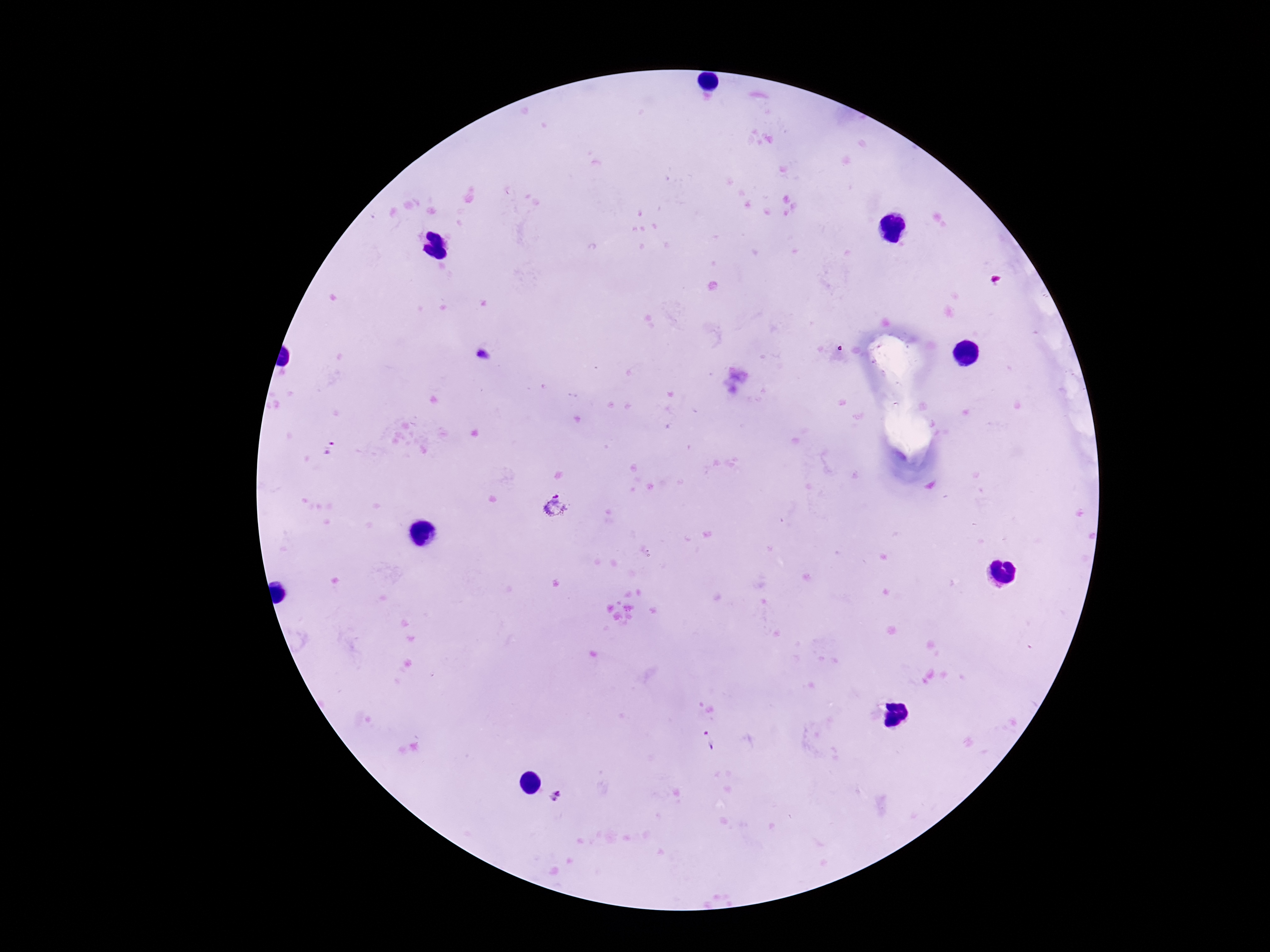

Approximate object centers, in pixels from the top-left corner.
Summary:
  - Plasmodium parasite locations: (x=482, y=356), (x=554, y=506), (x=709, y=740), (x=557, y=795)
  - Field of view: one from this slide
  - Patient malaria status: positive
  - Magnification: 100x
  - Preparation: thick peripheral-blood smear
  - Stain: Giemsa
  - Capture: smartphone camera through the microscope eyepiece
  - Image size: 1270×952 pixels